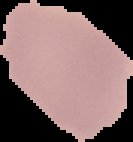
Summary:
  - Image size: 133×142 pixels
  - Result: no Plasmodium parasites detected
  - Image type: cell region segmented out of the field of view; surrounding area masked to black
  - Preparation: thin blood film